Assess this cell for malaria.
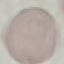
It is uninfected.

Thin blood film. Automatically extracted cell patch, resized to 64 × 64 pixels. Giemsa-stained preparation. Photographed with a smartphone camera at the microscope eyepiece.